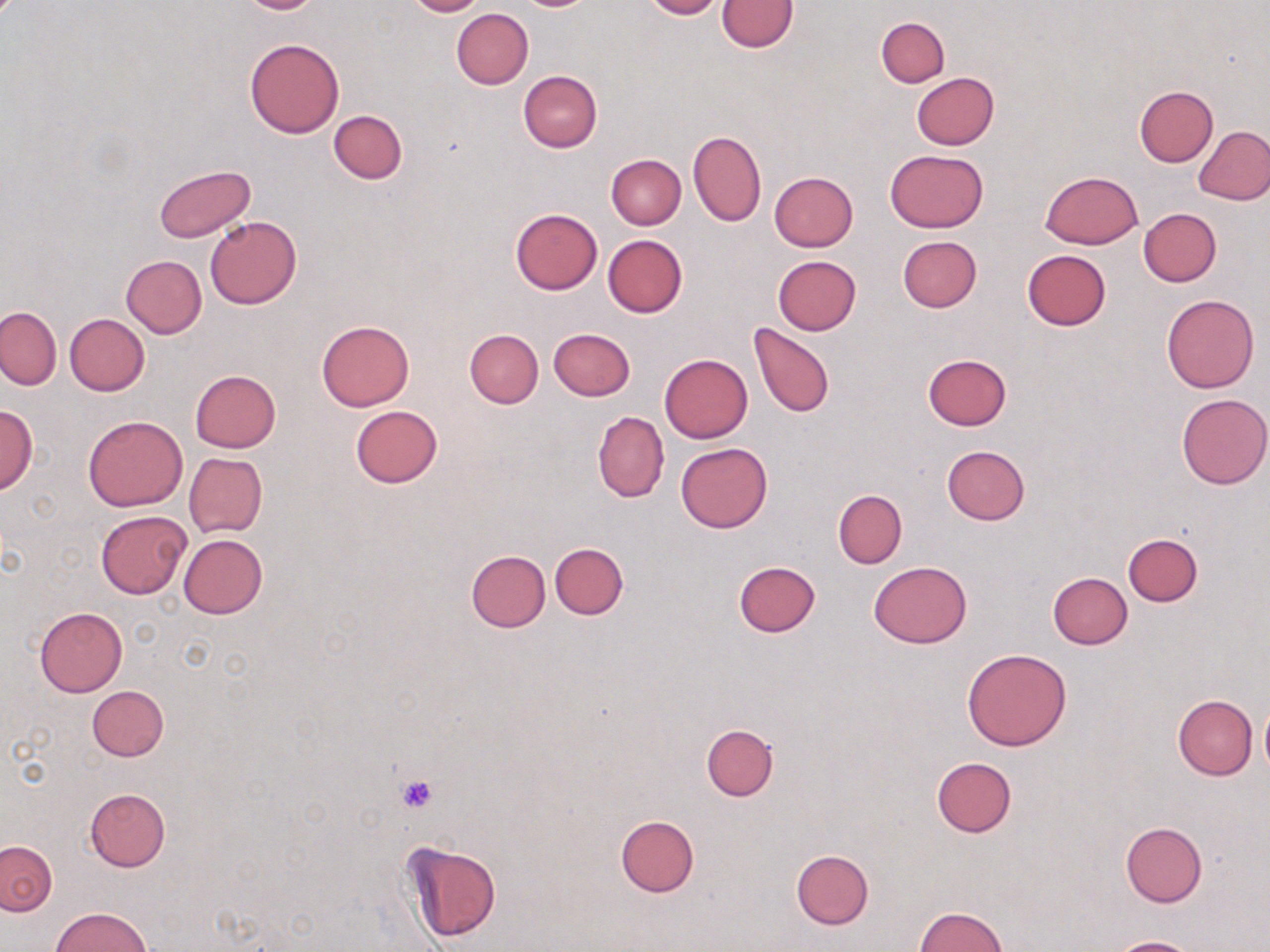
Summary:
  - Coordinate format: approximate bounding boxes as (x1, y1, x2, y2) in pixels
  - Uninfected red blood cell locations: (233, 0, 325, 14), (405, 0, 488, 17), (642, 0, 725, 19), (717, 0, 797, 52), (451, 8, 533, 89), (876, 17, 949, 87), (244, 38, 345, 138), (518, 69, 602, 152), (911, 72, 999, 150), (1135, 85, 1219, 166), (329, 111, 408, 183), (1195, 125, 1270, 205), (687, 130, 766, 227), (885, 149, 988, 232), (607, 154, 685, 229), (154, 165, 255, 243), (1039, 171, 1143, 249), (769, 172, 858, 252), (1138, 207, 1221, 287), (510, 209, 603, 295), (204, 215, 302, 309), (603, 234, 688, 317), (898, 237, 981, 312), (1023, 249, 1111, 330), (120, 255, 207, 337), (771, 255, 862, 335), (1162, 295, 1259, 393), (0, 307, 61, 389), (65, 313, 149, 395), (317, 320, 414, 411), (748, 322, 834, 418), (548, 327, 635, 401), (464, 331, 543, 408), (660, 353, 752, 442), (922, 354, 1011, 431), (190, 370, 281, 452), (1176, 394, 1270, 489), (0, 405, 38, 493), (351, 405, 442, 487), (592, 411, 669, 503), (84, 415, 188, 511), (676, 442, 773, 533), (941, 445, 1030, 526), (184, 453, 267, 537), (833, 490, 906, 568), (96, 511, 191, 599), (1122, 533, 1202, 606), (179, 534, 268, 619), (550, 543, 628, 619), (465, 550, 551, 632), (733, 561, 820, 637), (869, 561, 972, 648), (1048, 572, 1132, 648), (35, 607, 127, 696), (962, 648, 1072, 750), (87, 686, 169, 762), (1173, 693, 1257, 780), (1259, 701, 1270, 775), (701, 723, 779, 802), (930, 756, 1016, 838), (84, 788, 171, 872), (614, 815, 699, 896), (1119, 822, 1207, 907), (402, 840, 501, 943), (1, 841, 56, 915), (792, 849, 874, 929), (52, 906, 152, 952), (914, 906, 1007, 952), (1104, 936, 1200, 952)
  - Platelet locations: (397, 774, 437, 813)
  - Slide-level diagnosis: no evidence of blood parasites
  - Preparation: thin blood smear
  - Magnification: 1000x
  - Stain: May-Grünwald-Giemsa
  - Modality: optical microscopy
  - Image size: 1270×952 pixels
  - Field of view: single